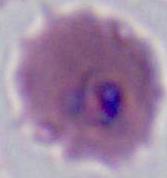

Summary:
  - Identification: Plasmodium
  - Magnification: 400x or 1000x
  - Modality: photomicrograph